Name the parasite shown.
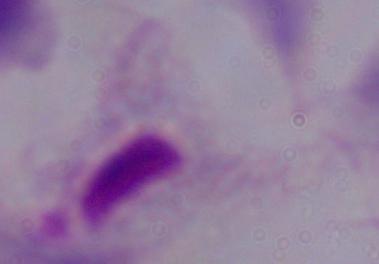
This is a trichomonad.

Summary:
  - Magnification: 1000x
  - Modality: photomicrograph